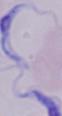

magnification = 1000x
modality = photomicrograph
identification = trypanosome